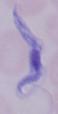
identification: trypanosome
magnification: 1000x
modality: micrograph